Classify this cell by malaria status.
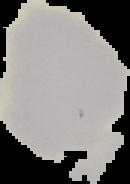
It is uninfected.

From a thin blood smear. Segmented cell region on a black background. Image is 130×184 pixels.